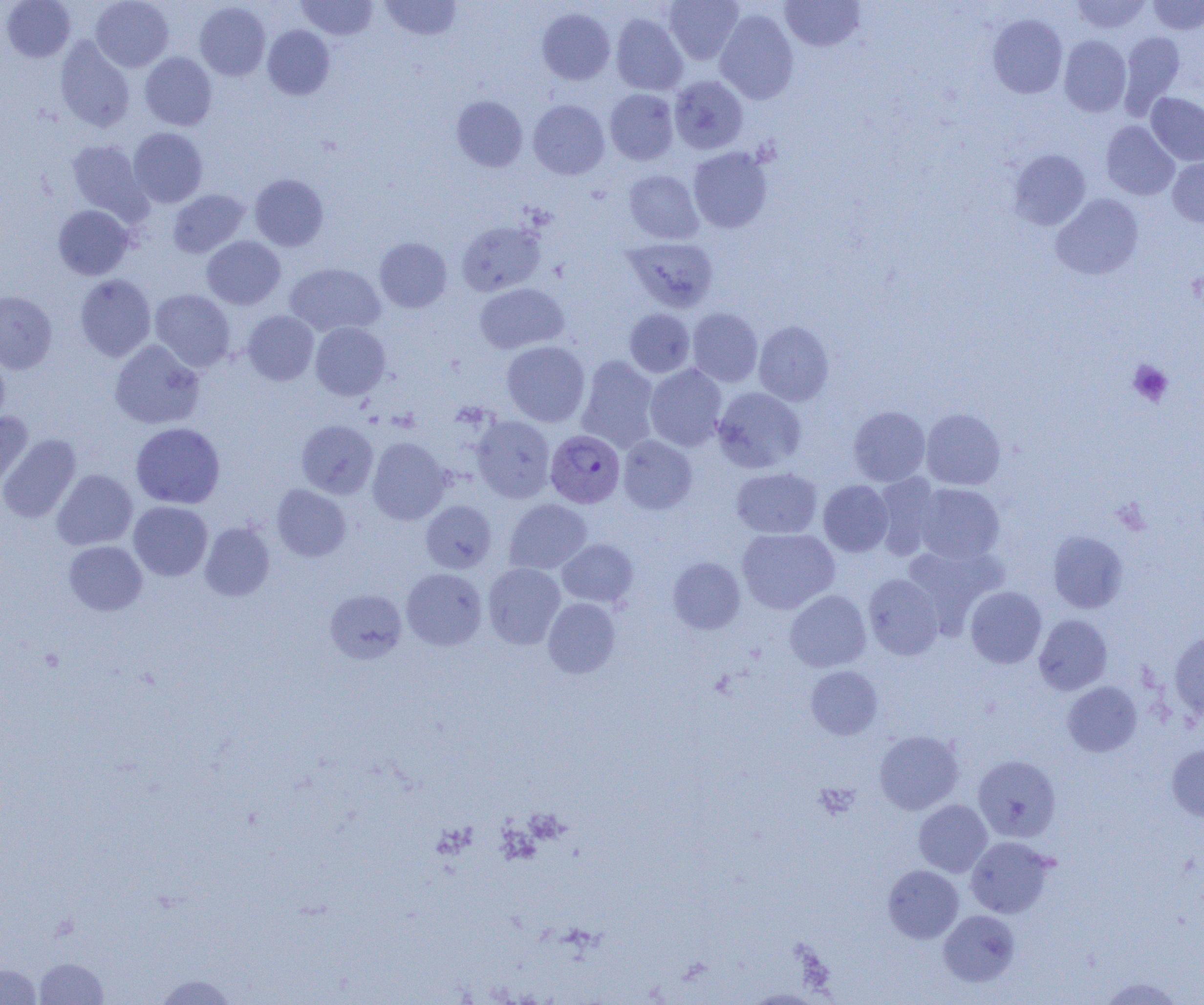

Summary:
  - Coordinate format: approximate bounding boxes as (x1,y1)-(x2,y2) corner pairs in pixels
  - Plasmodium vivax-infected red blood cell locations: (546,430)-(624,508)
  - Platelet locations: (1128,360)-(1173,406), (814,783)-(859,820)
  - Uninfected red blood cell locations: (1,0)-(75,61), (91,0)-(173,72), (379,0)-(462,41), (664,0)-(744,64), (780,0)-(865,51), (1072,0)-(1151,33), (1148,0)-(1204,34), (296,1)-(378,40), (195,2)-(270,81), (537,8)-(615,85), (714,8)-(799,104), (610,13)-(688,95), (987,14)-(1067,98), (263,25)-(335,100), (1119,31)-(1185,118), (1059,35)-(1131,117), (55,38)-(135,132), (140,52)-(217,130), (669,75)-(748,154), (604,89)-(679,165), (1146,92)-(1204,166), (452,95)-(528,172), (529,99)-(609,179), (1101,121)-(1180,200), (128,127)-(208,208), (66,140)-(149,220), (688,147)-(773,233), (1008,149)-(1091,230), (1167,156)-(1204,227), (623,170)-(703,244), (249,174)-(329,250), (168,189)-(250,258), (1051,193)-(1143,280), (53,205)-(134,280), (456,220)-(546,296), (202,236)-(285,309), (623,237)-(719,312), (375,238)-(452,312), (285,262)-(385,337), (75,274)-(156,361), (474,283)-(568,353), (150,289)-(236,371), (0,291)-(57,374), (688,307)-(763,386), (624,308)-(695,377), (242,310)-(319,385), (754,320)-(834,405), (310,322)-(390,400), (109,340)-(205,429), (124,340)-(212,507), (501,341)-(590,427), (0,352)-(10,428), (576,355)-(660,452), (645,364)-(726,451), (713,386)-(806,473), (848,406)-(930,486), (921,408)-(1005,490), (0,413)-(33,492), (472,415)-(556,503), (297,420)-(378,498), (131,422)-(225,509), (0,434)-(80,523), (618,435)-(697,513), (367,437)-(451,524), (731,467)-(822,539), (52,469)-(137,550), (873,473)-(942,559), (818,480)-(893,557), (914,483)-(1005,565), (272,484)-(351,561), (504,499)-(592,574), (421,500)-(497,573), (129,501)-(212,581), (200,522)-(275,601), (736,528)-(839,614), (1048,530)-(1128,613), (557,539)-(638,607), (64,541)-(147,615), (903,545)-(1006,631), (667,557)-(745,634), (483,563)-(565,649), (401,568)-(487,650), (863,573)-(944,660), (965,586)-(1046,669), (325,589)-(407,663), (785,590)-(871,672), (543,597)-(621,678), (1034,614)-(1112,694), (1169,632)-(1204,719), (805,665)-(882,739), (1062,681)-(1141,756), (874,730)-(963,815), (1167,744)-(1204,821), (973,755)-(1060,842), (914,800)-(992,877), (966,836)-(1055,918), (883,865)-(963,943), (938,909)-(1019,987), (34,957)-(110,1004), (0,963)-(43,1005), (152,973)-(241,1005), (1098,976)-(1185,1004), (744,989)-(825,1004)
  - Slide-level diagnosis: Plasmodium vivax
  - Modality: optical microscopy
  - Field of view: single
  - Preparation: thin blood smear
  - Image size: 1204×1005 pixels
  - Magnification: 1000x